Outline each uninfected red blood cell.
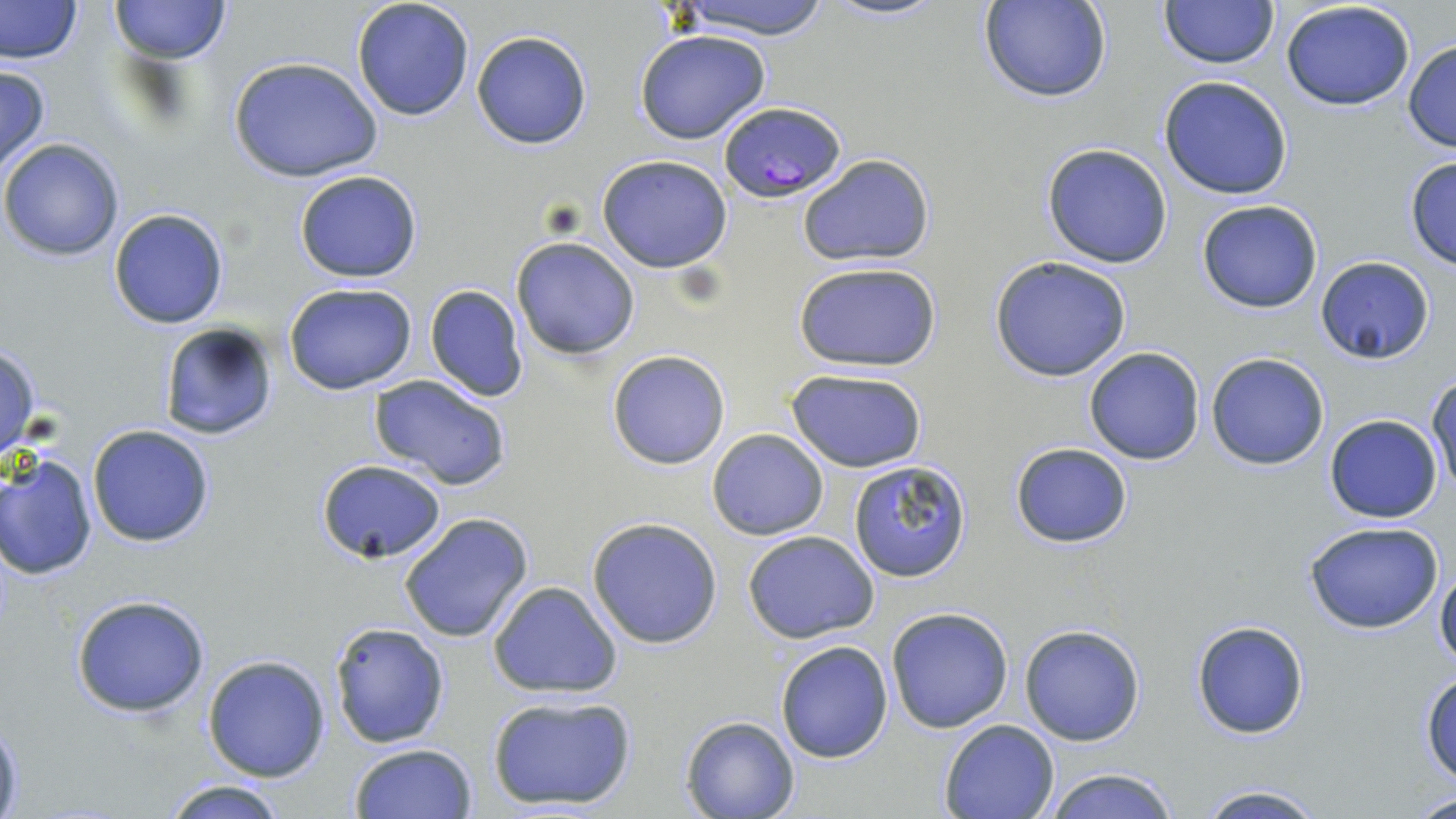

Approximate bounding boxes as named x1/y1/x2/y2 corners in pixels.
Uninfected red blood cells: (x1=0, y1=0, x2=83, y2=65), (x1=111, y1=0, x2=229, y2=65), (x1=351, y1=0, x2=475, y2=121), (x1=669, y1=0, x2=835, y2=41), (x1=825, y1=0, x2=944, y2=22), (x1=979, y1=0, x2=1112, y2=103), (x1=1159, y1=0, x2=1276, y2=69), (x1=1279, y1=0, x2=1416, y2=112), (x1=471, y1=29, x2=593, y2=149), (x1=635, y1=30, x2=772, y2=145), (x1=1403, y1=39, x2=1456, y2=152), (x1=229, y1=56, x2=383, y2=183), (x1=0, y1=65, x2=51, y2=175), (x1=1158, y1=76, x2=1293, y2=201), (x1=1, y1=137, x2=125, y2=262), (x1=1040, y1=142, x2=1173, y2=269), (x1=594, y1=154, x2=735, y2=274), (x1=797, y1=154, x2=935, y2=267), (x1=1402, y1=155, x2=1456, y2=269), (x1=293, y1=169, x2=423, y2=282), (x1=1196, y1=200, x2=1324, y2=313), (x1=109, y1=208, x2=228, y2=328), (x1=511, y1=236, x2=640, y2=359), (x1=989, y1=256, x2=1132, y2=381), (x1=1315, y1=256, x2=1435, y2=364), (x1=792, y1=260, x2=942, y2=374), (x1=282, y1=281, x2=418, y2=394), (x1=425, y1=284, x2=530, y2=402), (x1=157, y1=321, x2=280, y2=442), (x1=0, y1=342, x2=41, y2=462), (x1=1083, y1=348, x2=1205, y2=465), (x1=606, y1=349, x2=731, y2=470), (x1=1204, y1=352, x2=1331, y2=470), (x1=785, y1=369, x2=928, y2=473), (x1=368, y1=375, x2=513, y2=492), (x1=1427, y1=376, x2=1456, y2=499), (x1=1324, y1=415, x2=1442, y2=522), (x1=86, y1=424, x2=216, y2=548), (x1=706, y1=427, x2=830, y2=540), (x1=1009, y1=441, x2=1133, y2=548), (x1=2, y1=454, x2=99, y2=580), (x1=315, y1=459, x2=448, y2=565), (x1=849, y1=460, x2=974, y2=582), (x1=399, y1=513, x2=535, y2=643), (x1=587, y1=517, x2=726, y2=649), (x1=1302, y1=521, x2=1447, y2=635), (x1=742, y1=530, x2=881, y2=643), (x1=1435, y1=556, x2=1456, y2=671), (x1=487, y1=580, x2=623, y2=700), (x1=71, y1=596, x2=211, y2=718), (x1=885, y1=606, x2=1015, y2=733), (x1=1191, y1=620, x2=1309, y2=738), (x1=329, y1=621, x2=451, y2=750), (x1=1019, y1=624, x2=1146, y2=746), (x1=773, y1=640, x2=894, y2=763), (x1=203, y1=654, x2=331, y2=781), (x1=1420, y1=670, x2=1456, y2=784), (x1=486, y1=693, x2=637, y2=812), (x1=0, y1=712, x2=23, y2=817), (x1=681, y1=715, x2=799, y2=818), (x1=938, y1=718, x2=1060, y2=819), (x1=348, y1=743, x2=477, y2=819), (x1=1041, y1=766, x2=1180, y2=819), (x1=156, y1=778, x2=295, y2=818), (x1=1190, y1=782, x2=1329, y2=819), (x1=1412, y1=789, x2=1456, y2=819).

slide_level_diagnosis: Plasmodium falciparum
field_of_view: single
magnification: 1000x
plasmodium_falciparum_infected_red_blood_cell_locations: 'approximate bounding boxes as named x1/y1/x2/y2 corners in pixels: (x1=720, y1=100, x2=847, y2=202)'
modality: light microscopy
preparation: thin blood film
stain: May-Grünwald-Giemsa
image_size: 1456×819 pixels